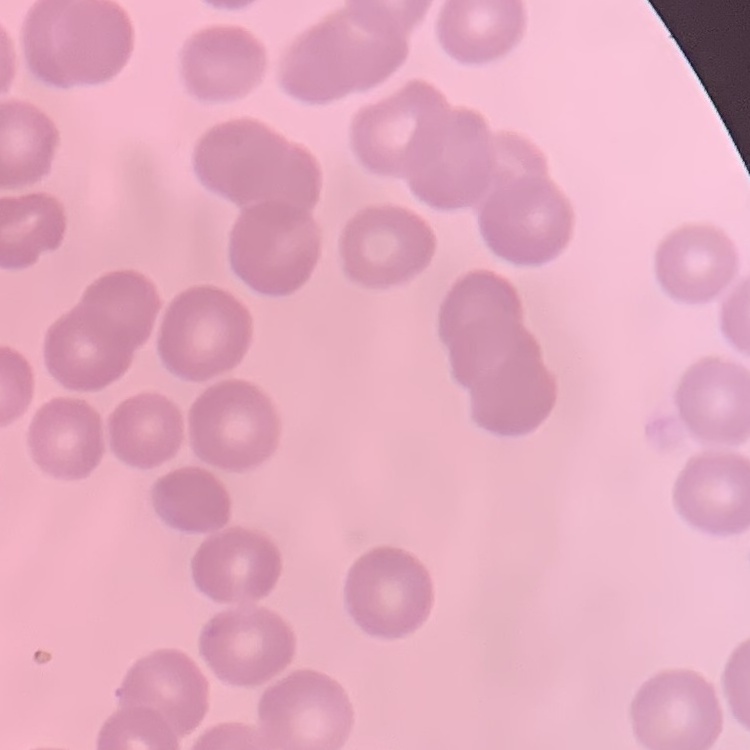
The red blood cells show no rouleaux formation. One tile cut from a larger photomicrograph. Field's or Giemsa stain. Thin peripheral smear.